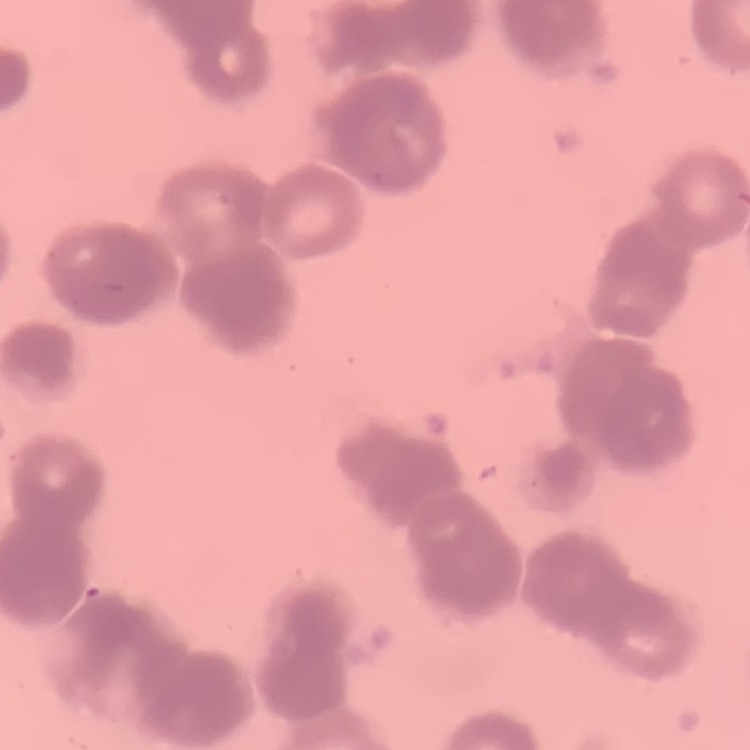 The red blood cells show rouleaux formation. One tile cut from a larger photomicrograph. Stained with either Field's or Giemsa. Thin blood film.